Identify the preparation type.
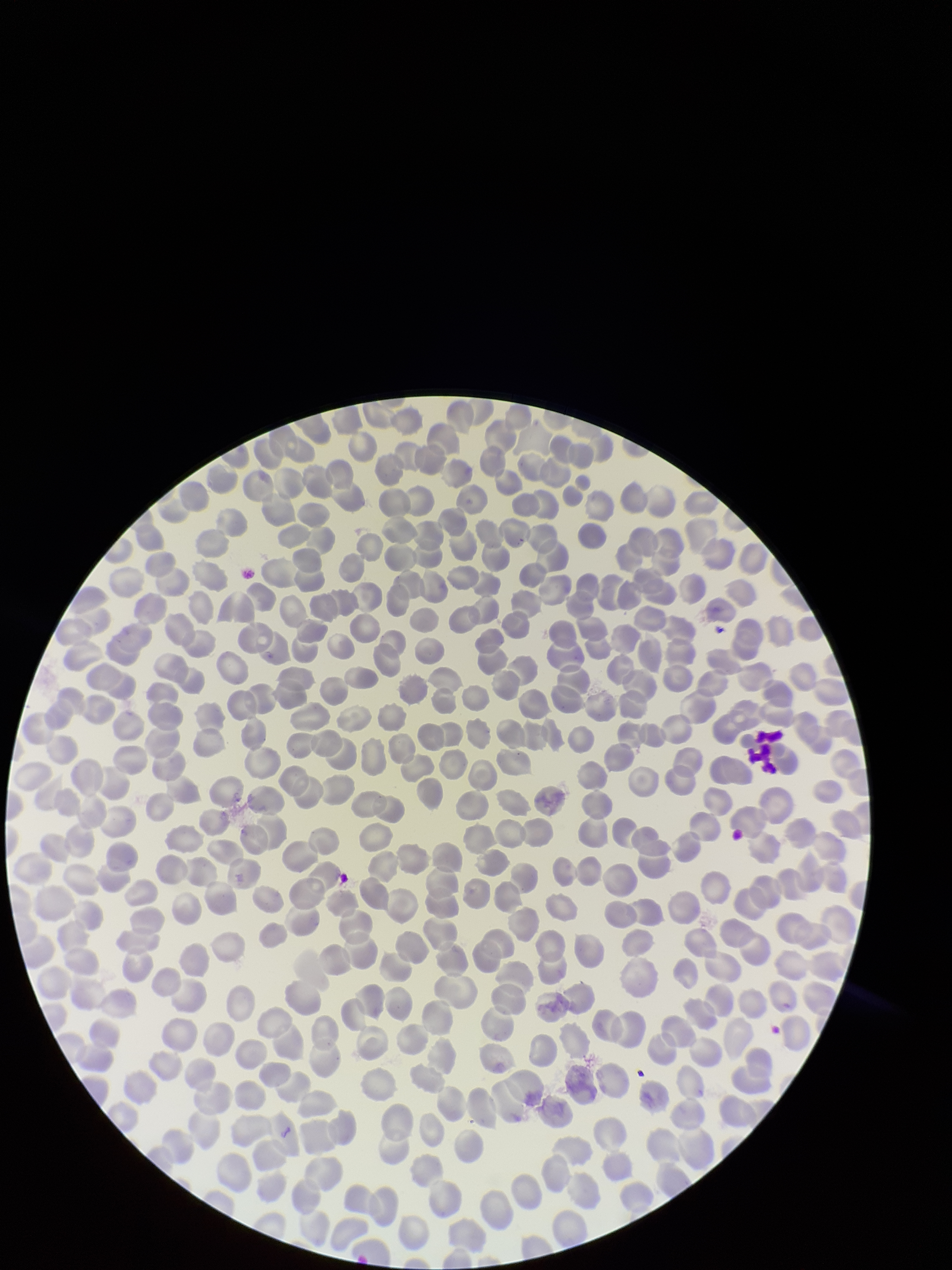

A thin smear.

Parasitized red blood cell count: 0. Image is 952×1270 pixels. Photographed through the microscope eyepiece with a smartphone camera. Single field of view. Parasitized red blood cells: none identified. Red blood cell count: 370. Patient malaria status: negative. Stained with Giemsa.